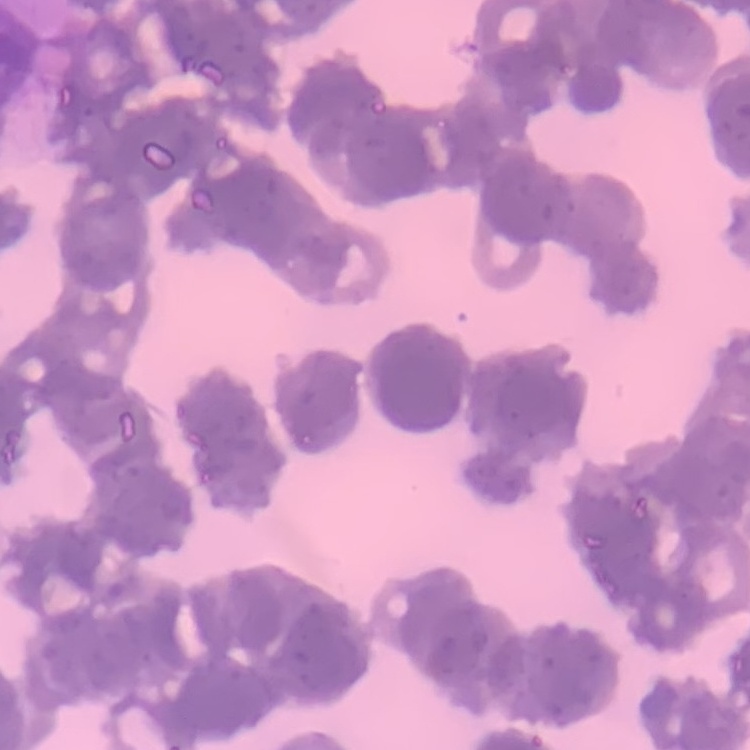

The red blood cells exhibit rouleaux formation. Square crop of a larger photomicrograph. Thin peripheral smear. Field's or Giemsa stain.